Report the malaria status of this cell.
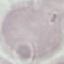

Uninfected.

Thin blood smear. Acquired by smartphone through the microscope eyepiece. Giemsa-stained preparation. Automatically extracted cell patch, resized to 64 × 64 pixels.